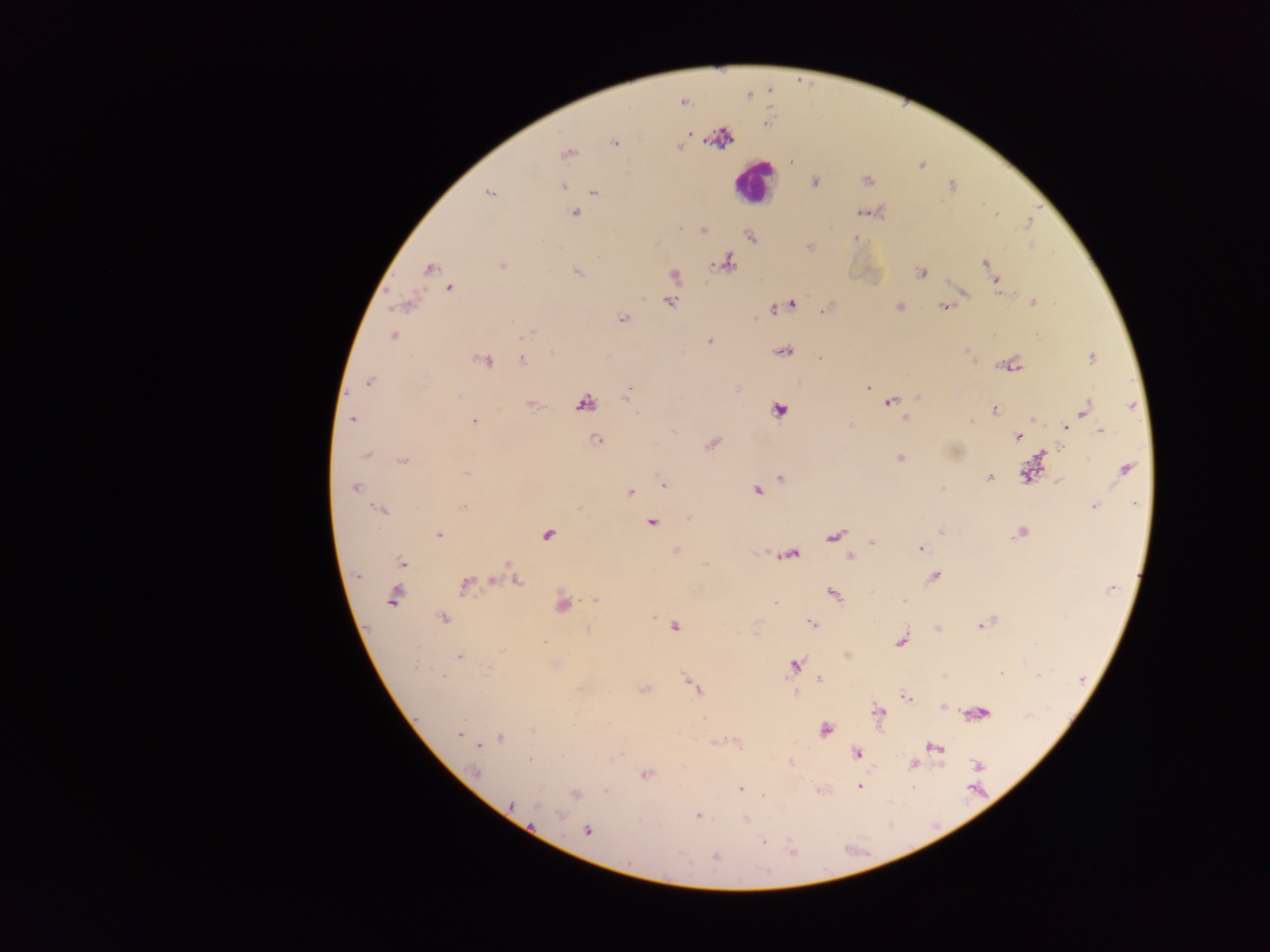

image_size: 1270×952 pixels
preparation: thick blood film
leukocyte_locations: 'approximate centers as {x, y} in pixels: {753, 181}'
malaria_parasite_locations: 'approximate centers as {x, y} in pixels: {749, 95}, {683, 102}, {688, 133}, {615, 142}, {679, 146}, {567, 153}, {814, 182}, {564, 186}, {594, 191}, {489, 193}, {860, 213}, {574, 214}, {680, 228}, {703, 230}, {750, 237}, {854, 238}, {727, 263}, {985, 263}, {503, 266}, {430, 268}, {576, 272}, {921, 272}, {991, 272}, {674, 275}, {996, 281}, {450, 288}, {669, 302}, {1034, 303}, {791, 304}, {405, 305}, {900, 307}, {944, 307}, {774, 309}, {622, 318}, {529, 333}, {393, 336}, {709, 341}, {783, 352}, {819, 358}, {1091, 358}, {522, 360}, {486, 361}, {368, 382}, {867, 387}, {626, 397}, {917, 398}, {890, 402}, {584, 404}, {531, 405}, {1132, 406}, {779, 409}, {1084, 410}, {995, 411}, {905, 418}, {351, 420}, {474, 421}, {971, 421}, {1066, 427}, {1101, 432}, {1017, 437}, {597, 441}, {712, 444}, {1042, 454}, {366, 455}, {900, 458}, {402, 461}, {1125, 470}, {465, 474}, {1025, 475}, {989, 477}, {780, 478}, {1059, 481}, {663, 483}, {355, 488}, {942, 489}, {757, 491}, {630, 492}, {1135, 505}, {1094, 507}, {463, 508}, {381, 510}, {651, 522}, {940, 532}, {1021, 533}, {548, 534}, {439, 535}, {834, 536}, {872, 542}, {920, 548}, {676, 550}, {790, 554}, {850, 557}, {401, 562}, {510, 566}, {358, 576}, {935, 576}, {494, 580}, {517, 580}, {465, 585}, {1113, 589}, {833, 594}, {393, 596}, {904, 600}, {595, 601}, {563, 605}, {443, 618}, {812, 623}, {982, 624}, {674, 627}, {588, 630}, {901, 641}, {544, 642}, {501, 650}, {460, 656}, {794, 665}, {1001, 674}, {443, 676}, {820, 680}, {695, 687}, {644, 689}, {796, 693}, {906, 698}, {943, 707}, {879, 713}, {980, 713}, {534, 731}, {826, 731}, {459, 734}, {500, 738}, {479, 746}, {935, 747}, {857, 754}, {529, 759}, {790, 762}, {913, 764}, {978, 765}, {476, 772}, {647, 775}, {859, 786}, {741, 789}, {606, 791}, {575, 795}, {512, 804}, {537, 808}, {560, 815}, {697, 816}, {746, 818}, {587, 832}, {764, 841}, {792, 852}, {715, 857}'
capture: mobile-phone photograph through a microscope
field_of_view: single
country: Ghana